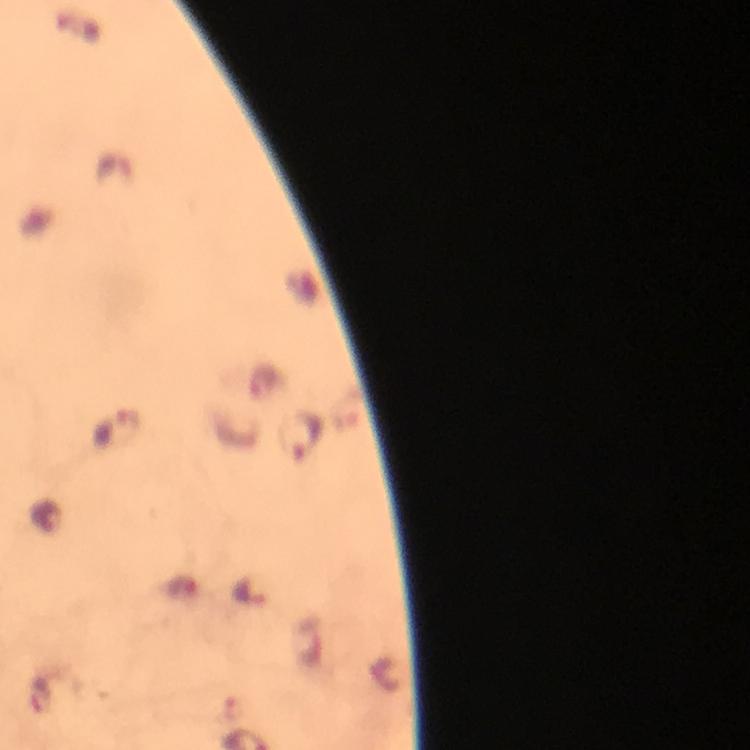
Approximate centers as {x, y} in pixels. Malaria parasite locations: {265, 383}, {115, 428}, {302, 434}, {47, 513}, {249, 592}. Thick blood film. A crop from one field of view. Photographed through the microscope with a smartphone camera. 100x magnification. Giemsa-stained preparation. From a diagnostic examination for malaria. Image is 750×750 pixels. Immersion oil was used.